Assess this cell for malaria.
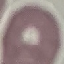

Uninfected.

Thin blood smear. Cell patch, automatically extracted from a larger field of view and resized to 64 × 64 pixels. Photographed with a smartphone camera at the microscope eyepiece. Giemsa stain.